Assess this cell for malaria.
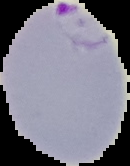

It is parasitized.

Summary:
  - Preparation: thin blood smear
  - Image size: 130×166 pixels
  - Image type: segmented cell region on a black background